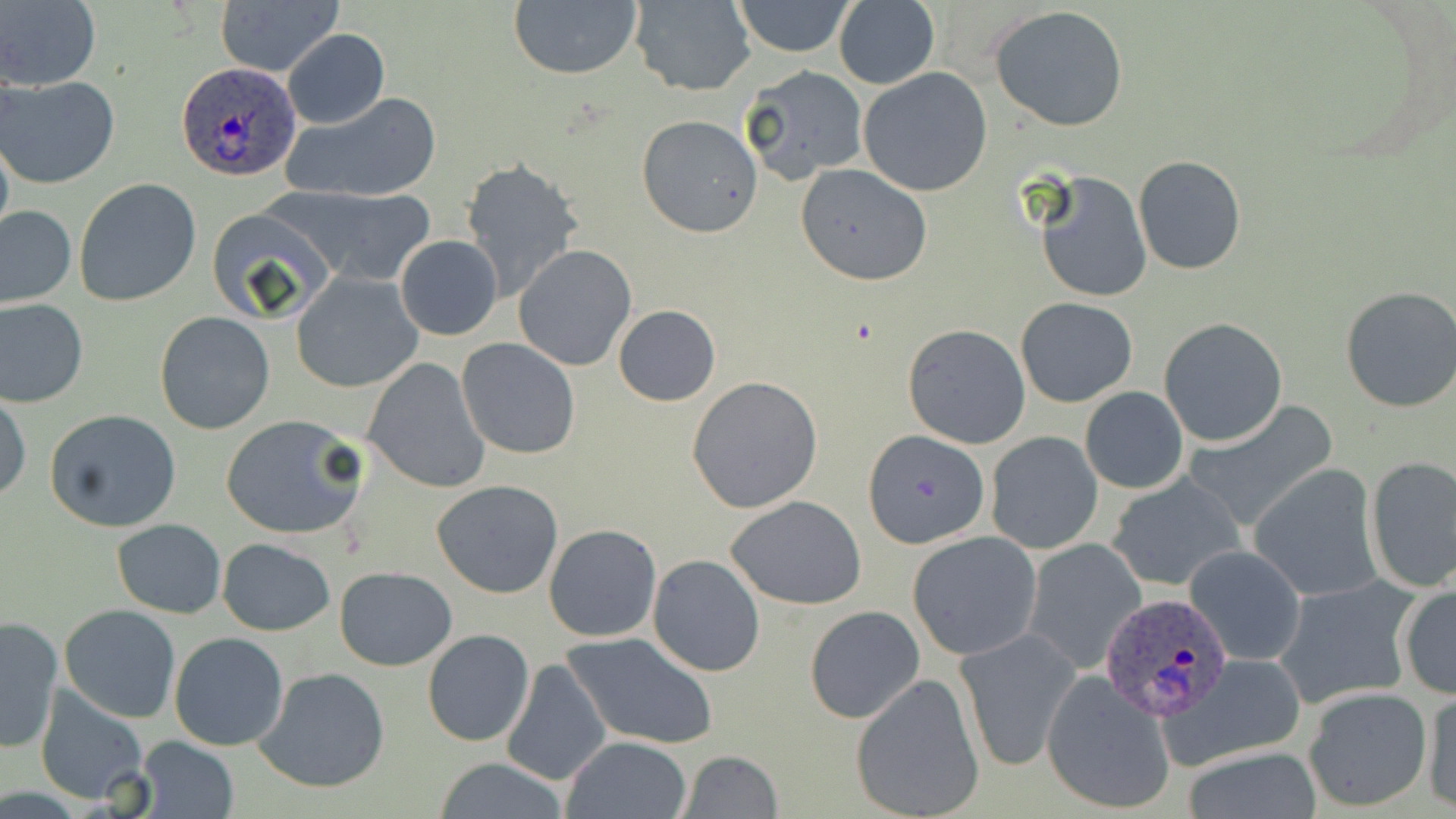

{
  "slide_level_diagnosis": "Plasmodium ovale",
  "field_of_view": "one of a larger specimen",
  "magnification": "1000x",
  "uninfected_red_blood_cell_locations": "approximate bounding boxes as (x1,y1)-(x2,y2) corner pairs in pixels: (216,0)-(343,78), (507,0)-(643,80), (1,1)-(101,91), (627,1)-(755,96), (729,1)-(857,56), (834,2)-(940,88), (990,5)-(1129,130), (284,29)-(389,129), (741,64)-(870,183), (859,68)-(993,197), (2,74)-(122,188), (280,91)-(441,204), (636,116)-(763,238), (1133,155)-(1246,274), (460,159)-(583,300), (795,162)-(933,285), (1036,171)-(1152,304), (74,179)-(202,305), (283,187)-(435,285), (0,205)-(76,309), (207,207)-(339,327), (395,235)-(504,340), (514,246)-(636,371), (290,271)-(423,394), (1339,285)-(1456,414), (1016,296)-(1138,408), (0,297)-(88,408), (612,305)-(721,406), (153,311)-(275,435), (1159,317)-(1289,447), (902,323)-(1031,449), (456,338)-(581,459), (361,358)-(490,494), (686,375)-(823,513), (1081,386)-(1188,494), (0,392)-(30,505), (1184,403)-(1337,532), (46,409)-(184,533), (220,413)-(367,540), (863,431)-(988,547), (986,432)-(1103,554), (1364,455)-(1456,593), (1249,464)-(1382,602), (1104,471)-(1245,594), (430,480)-(564,600), (726,495)-(867,608), (112,519)-(226,618), (543,524)-(663,643), (907,531)-(1042,660), (217,537)-(336,635), (1021,538)-(1146,675), (1185,545)-(1306,666), (648,554)-(765,677), (333,566)-(456,670), (1272,576)-(1419,710), (1397,579)-(1456,701), (59,604)-(182,723), (804,605)-(926,725), (0,615)-(63,754), (954,626)-(1083,772), (423,630)-(533,746), (169,632)-(289,750), (562,633)-(718,750), (1161,654)-(1310,770), (500,658)-(610,788), (253,668)-(390,794), (1041,671)-(1176,816), (850,672)-(986,819), (35,684)-(153,804), (1420,687)-(1456,813), (1303,688)-(1430,813), (134,736)-(239,819), (561,736)-(693,819), (1180,745)-(1323,819), (677,750)-(783,819), (431,758)-(572,817)",
  "plasmodium_ovale_infected_red_blood_cell_locations": "approximate bounding boxes as (x1,y1)-(x2,y2) corner pairs in pixels: (177,62)-(302,181), (1099,592)-(1234,722)",
  "modality": "optical microscopy",
  "stain": "May-Grünwald-Giemsa",
  "preparation": "thin blood smear",
  "image_size": "1456×819 pixels"
}